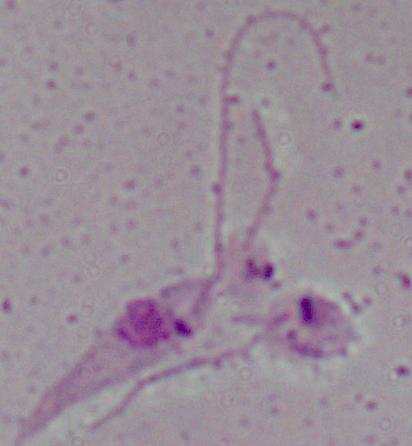
{
  "magnification": "1000x",
  "modality": "micrograph",
  "identification": "Leishmania"
}